Identify the parasite.
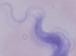

A trypanosome.

magnification = 1000x
modality = photomicrograph